Identify the cell.
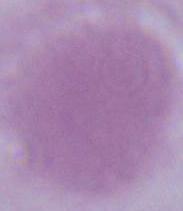
This is an erythrocyte.

magnification = 1000x
modality = micrograph